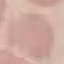

Summary:
  - Result: negative for malaria parasites
  - Image type: cell patch, automatically extracted from a larger field of view and resized to 64 × 64 pixels
  - Capture: smartphone through the microscope eyepiece
  - Stain: Giemsa
  - Preparation: thin smear